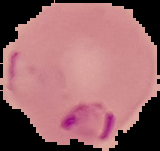

Malaria status: parasitized. The area outside the segmented cell region is set to black. From a thin blood film. Image is 160×151 pixels.